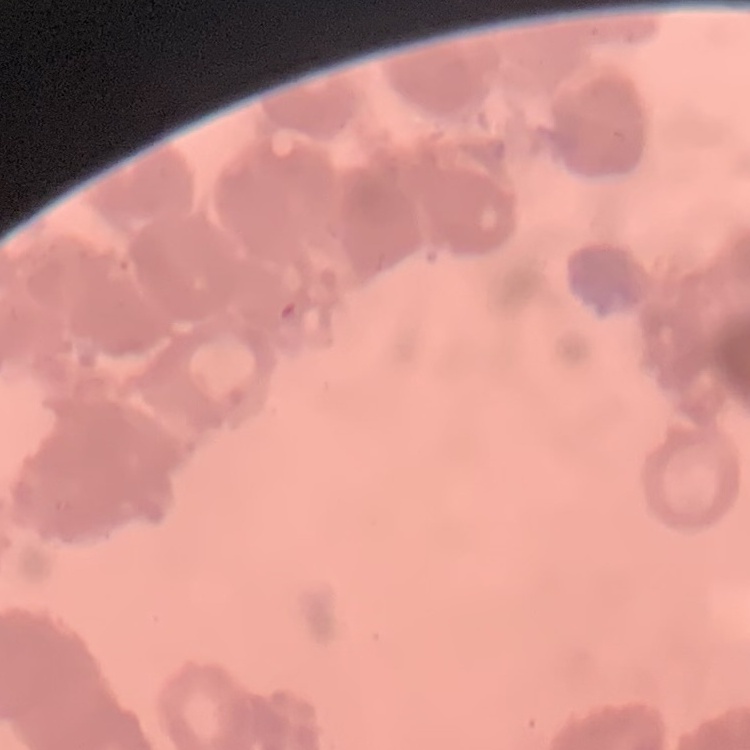
erythrocyte_morphology: rouleaux formation
image_type: square crop of a larger photomicrograph
preparation: thin blood film
stain: Field's or Giemsa